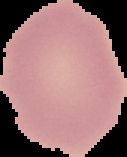

image_type: cell region segmented out of the field of view; surrounding area masked to black
result: no Plasmodium parasites seen
image_size: 127×157 pixels
preparation: thin blood smear